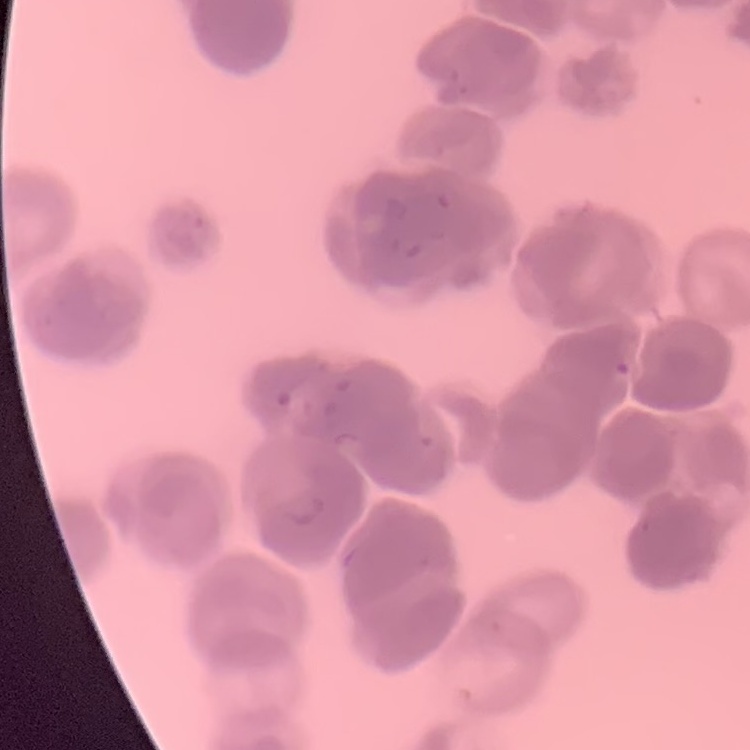

Summary:
  - Erythrocyte morphology: rouleaux formation
  - Image type: square crop of a larger photomicrograph
  - Stain: Field's or Giemsa
  - Preparation: thin peripheral smear